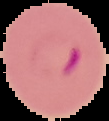
Summary:
  - Preparation: thin blood smear
  - Malaria status: parasitized
  - Image type: segmented cell region on a black background
  - Image size: 109×121 pixels